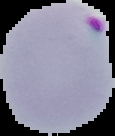
The area outside the segmented cell region is set to black. Result: malaria parasites detected. From a thin blood smear. Image is 115×136 pixels.